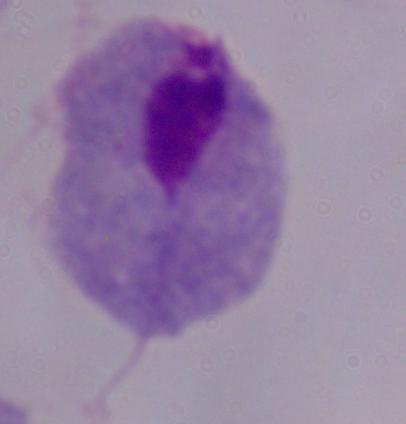
Micrograph. 1000x magnification. A trichomonad is shown.